Give the extent of all Plasmodium ovale-infected red blood cells.
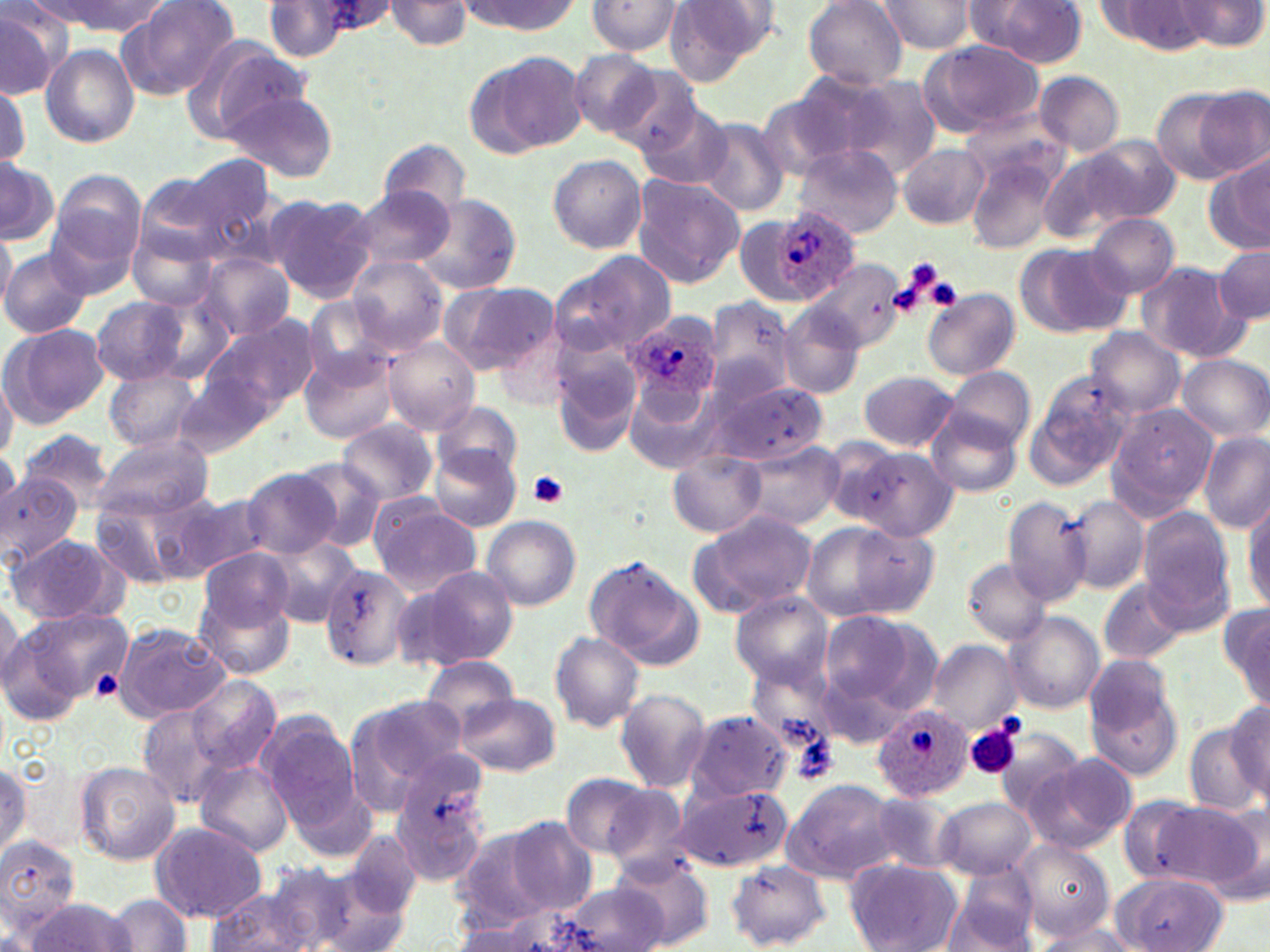

Approximate bounding boxes as named x1/y1/x2/y2 corners in pixels.
Plasmodium ovale-infected red blood cells: (x1=769, y1=206, x2=858, y2=304), (x1=626, y1=324, x2=721, y2=399), (x1=871, y1=705, x2=973, y2=800).

Uninfected red blood cell locations: (x1=48, y1=0, x2=166, y2=35), (x1=119, y1=0, x2=239, y2=98), (x1=262, y1=0, x2=354, y2=58), (x1=385, y1=0, x2=473, y2=50), (x1=803, y1=0, x2=909, y2=88), (x1=1177, y1=0, x2=1266, y2=51), (x1=0, y1=1, x2=72, y2=99), (x1=459, y1=1, x2=580, y2=34), (x1=586, y1=1, x2=684, y2=56), (x1=663, y1=1, x2=772, y2=84), (x1=874, y1=1, x2=982, y2=55), (x1=966, y1=1, x2=1087, y2=68), (x1=1100, y1=2, x2=1218, y2=54), (x1=916, y1=39, x2=1042, y2=136), (x1=200, y1=42, x2=310, y2=138), (x1=41, y1=44, x2=138, y2=148), (x1=569, y1=50, x2=665, y2=142), (x1=470, y1=52, x2=585, y2=157), (x1=611, y1=64, x2=702, y2=155), (x1=1035, y1=71, x2=1123, y2=156), (x1=843, y1=75, x2=943, y2=178), (x1=761, y1=82, x2=878, y2=181), (x1=0, y1=84, x2=28, y2=172), (x1=1152, y1=87, x2=1244, y2=183), (x1=223, y1=88, x2=338, y2=182), (x1=1195, y1=89, x2=1270, y2=177), (x1=638, y1=104, x2=732, y2=190), (x1=959, y1=109, x2=1068, y2=189), (x1=695, y1=118, x2=790, y2=217), (x1=1069, y1=132, x2=1182, y2=230), (x1=378, y1=138, x2=471, y2=218), (x1=794, y1=144, x2=902, y2=238), (x1=898, y1=144, x2=989, y2=229), (x1=183, y1=153, x2=283, y2=257), (x1=966, y1=153, x2=1061, y2=254), (x1=1037, y1=153, x2=1146, y2=244), (x1=548, y1=154, x2=647, y2=253), (x1=1205, y1=156, x2=1270, y2=257), (x1=0, y1=157, x2=58, y2=245), (x1=48, y1=173, x2=146, y2=284), (x1=135, y1=174, x2=230, y2=265), (x1=631, y1=176, x2=744, y2=288), (x1=347, y1=186, x2=454, y2=272), (x1=267, y1=195, x2=377, y2=302), (x1=415, y1=195, x2=519, y2=292), (x1=1085, y1=212, x2=1181, y2=299), (x1=736, y1=214, x2=790, y2=305), (x1=0, y1=227, x2=16, y2=314), (x1=127, y1=227, x2=220, y2=312), (x1=1014, y1=243, x2=1133, y2=339), (x1=1213, y1=245, x2=1270, y2=325), (x1=2, y1=248, x2=93, y2=338), (x1=547, y1=251, x2=675, y2=358), (x1=200, y1=254, x2=293, y2=340), (x1=348, y1=256, x2=448, y2=356), (x1=808, y1=257, x2=907, y2=354), (x1=1135, y1=262, x2=1247, y2=360), (x1=442, y1=282, x2=557, y2=373), (x1=924, y1=289, x2=1019, y2=379), (x1=141, y1=295, x2=237, y2=387), (x1=90, y1=297, x2=187, y2=383), (x1=305, y1=297, x2=394, y2=384), (x1=704, y1=297, x2=794, y2=397), (x1=780, y1=308, x2=861, y2=400), (x1=494, y1=311, x2=577, y2=412), (x1=202, y1=315, x2=319, y2=417), (x1=3, y1=322, x2=108, y2=425), (x1=1085, y1=327, x2=1184, y2=420), (x1=384, y1=338, x2=480, y2=435), (x1=551, y1=345, x2=642, y2=458), (x1=300, y1=349, x2=397, y2=444), (x1=1178, y1=354, x2=1269, y2=441), (x1=106, y1=365, x2=201, y2=453), (x1=944, y1=367, x2=1035, y2=450), (x1=0, y1=371, x2=16, y2=464), (x1=858, y1=372, x2=958, y2=452), (x1=1029, y1=372, x2=1133, y2=485), (x1=175, y1=374, x2=268, y2=458), (x1=702, y1=379, x2=829, y2=467), (x1=628, y1=383, x2=722, y2=473), (x1=432, y1=402, x2=522, y2=482), (x1=1107, y1=404, x2=1216, y2=517), (x1=928, y1=409, x2=1023, y2=499), (x1=340, y1=420, x2=438, y2=507), (x1=20, y1=429, x2=116, y2=509), (x1=1199, y1=433, x2=1269, y2=532), (x1=94, y1=436, x2=215, y2=520), (x1=738, y1=443, x2=843, y2=531), (x1=431, y1=445, x2=522, y2=532), (x1=847, y1=448, x2=957, y2=540), (x1=669, y1=452, x2=764, y2=537), (x1=295, y1=461, x2=385, y2=549), (x1=241, y1=467, x2=341, y2=559), (x1=0, y1=471, x2=84, y2=562), (x1=92, y1=493, x2=203, y2=591), (x1=174, y1=493, x2=274, y2=578), (x1=1001, y1=495, x2=1092, y2=606), (x1=1062, y1=496, x2=1149, y2=595), (x1=1244, y1=498, x2=1270, y2=610), (x1=368, y1=501, x2=481, y2=594), (x1=1136, y1=507, x2=1235, y2=617), (x1=692, y1=511, x2=818, y2=614), (x1=481, y1=515, x2=580, y2=611), (x1=805, y1=520, x2=940, y2=622), (x1=6, y1=534, x2=126, y2=627), (x1=261, y1=537, x2=361, y2=627), (x1=201, y1=548, x2=292, y2=632), (x1=582, y1=556, x2=702, y2=669), (x1=963, y1=560, x2=1050, y2=645), (x1=322, y1=561, x2=422, y2=674), (x1=398, y1=564, x2=520, y2=672), (x1=1100, y1=578, x2=1187, y2=664), (x1=198, y1=592, x2=295, y2=682), (x1=731, y1=592, x2=833, y2=689), (x1=0, y1=595, x2=23, y2=689), (x1=1220, y1=606, x2=1269, y2=709), (x1=816, y1=608, x2=932, y2=733), (x1=3, y1=610, x2=124, y2=718), (x1=1006, y1=613, x2=1104, y2=714), (x1=114, y1=624, x2=228, y2=723), (x1=550, y1=632, x2=644, y2=731), (x1=927, y1=641, x2=1019, y2=733), (x1=421, y1=657, x2=520, y2=735), (x1=1083, y1=668, x2=1188, y2=784), (x1=186, y1=675, x2=281, y2=774), (x1=614, y1=687, x2=711, y2=792), (x1=345, y1=694, x2=470, y2=808), (x1=458, y1=695, x2=561, y2=775), (x1=1226, y1=700, x2=1269, y2=802), (x1=137, y1=705, x2=230, y2=810), (x1=683, y1=710, x2=793, y2=805), (x1=257, y1=717, x2=364, y2=829), (x1=1183, y1=722, x2=1267, y2=814), (x1=1025, y1=755, x2=1137, y2=854), (x1=392, y1=756, x2=493, y2=879), (x1=0, y1=759, x2=29, y2=860), (x1=196, y1=760, x2=295, y2=859), (x1=75, y1=761, x2=181, y2=867), (x1=559, y1=774, x2=660, y2=860), (x1=781, y1=780, x2=902, y2=884), (x1=668, y1=785, x2=793, y2=873), (x1=863, y1=792, x2=959, y2=876), (x1=935, y1=797, x2=1037, y2=879), (x1=1167, y1=801, x2=1266, y2=896), (x1=504, y1=818, x2=597, y2=915), (x1=151, y1=822, x2=266, y2=921), (x1=452, y1=824, x2=565, y2=928), (x1=341, y1=829, x2=422, y2=919), (x1=0, y1=834, x2=80, y2=938), (x1=1016, y1=839, x2=1112, y2=941), (x1=608, y1=851, x2=715, y2=951), (x1=844, y1=858, x2=961, y2=952), (x1=729, y1=862, x2=829, y2=948), (x1=945, y1=867, x2=1040, y2=952), (x1=1114, y1=871, x2=1230, y2=951), (x1=205, y1=879, x2=351, y2=952), (x1=559, y1=881, x2=672, y2=952), (x1=105, y1=895, x2=195, y2=952), (x1=23, y1=898, x2=137, y2=951), (x1=1034, y1=923, x2=1141, y2=952). Platelet locations: (x1=910, y1=263, x2=956, y2=306), (x1=924, y1=277, x2=962, y2=309), (x1=529, y1=471, x2=570, y2=508), (x1=967, y1=724, x2=1020, y2=780), (x1=794, y1=734, x2=840, y2=782). Slide-level diagnosis: Plasmodium ovale. May-Grünwald-Giemsa stain. Light microscopy. Single field of view. Thin blood film. Captured at 1000x magnification. Image is 1270×952 pixels.